Assess this cell for malaria.
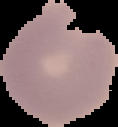
Parasitized.

image type = segmented cell region with the area outside set to black
preparation = thin blood film
image size = 118×127 pixels